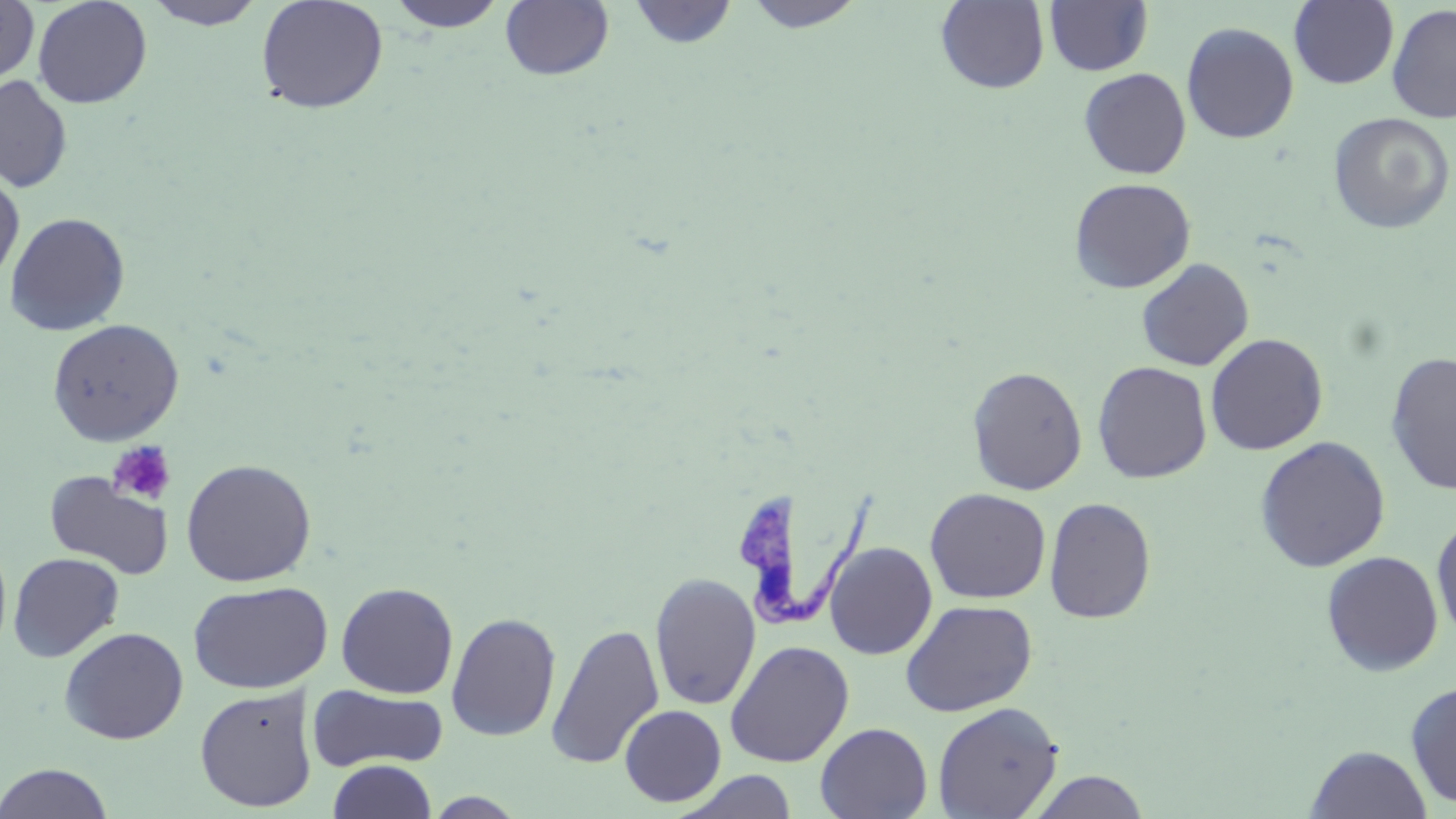 Approximate bounding boxes as (x1,y1)-(x2,y2) corner pairs in pixels. Trypanosoma brucei locations: (735,485)-(893,640). Platelet locations: (107,440)-(176,507). Uninfected red blood cell locations: (0,0)-(39,86), (32,0)-(153,109), (143,0)-(267,30), (255,0)-(389,115), (385,0)-(511,33), (742,0)-(867,33), (499,1)-(615,81), (627,1)-(738,49), (935,1)-(1050,94), (1043,1)-(1153,76), (1289,1)-(1399,89), (1386,4)-(1456,123), (1181,22)-(1299,144), (1079,68)-(1191,179), (0,75)-(73,193), (1328,112)-(1454,235), (0,169)-(24,288), (1069,177)-(1196,293), (4,212)-(131,336), (1136,258)-(1254,372), (46,318)-(185,446), (1205,333)-(1328,455), (1385,352)-(1456,495), (1091,361)-(1213,484), (966,366)-(1088,495), (1254,436)-(1391,573), (180,458)-(317,587), (44,472)-(173,580), (924,488)-(1052,603), (1043,496)-(1156,623), (1431,513)-(1456,643), (824,542)-(937,660), (1320,550)-(1443,676), (7,552)-(125,662), (649,572)-(761,712), (187,580)-(333,694), (335,582)-(458,698), (901,599)-(1038,717), (446,612)-(561,742), (546,623)-(665,769), (59,626)-(189,744), (725,640)-(855,767), (1405,680)-(1456,810), (194,685)-(318,812), (308,685)-(448,771), (932,701)-(1063,818), (619,705)-(727,806), (815,722)-(933,819), (1305,744)-(1433,819), (327,760)-(438,819), (0,763)-(115,819), (675,770)-(800,819), (1027,770)-(1151,818), (422,792)-(529,818). Slide-level diagnosis: Trypanosoma brucei. Thin blood film. Light microscopy. 1000x magnification. May-Grünwald-Giemsa stain. One field of a larger specimen. Image is 1456×819 pixels.